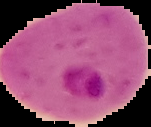

preparation = thin blood smear
image size = 151×127 pixels
image type = segmented cell region with the area outside set to black
result = Plasmodium parasites detected